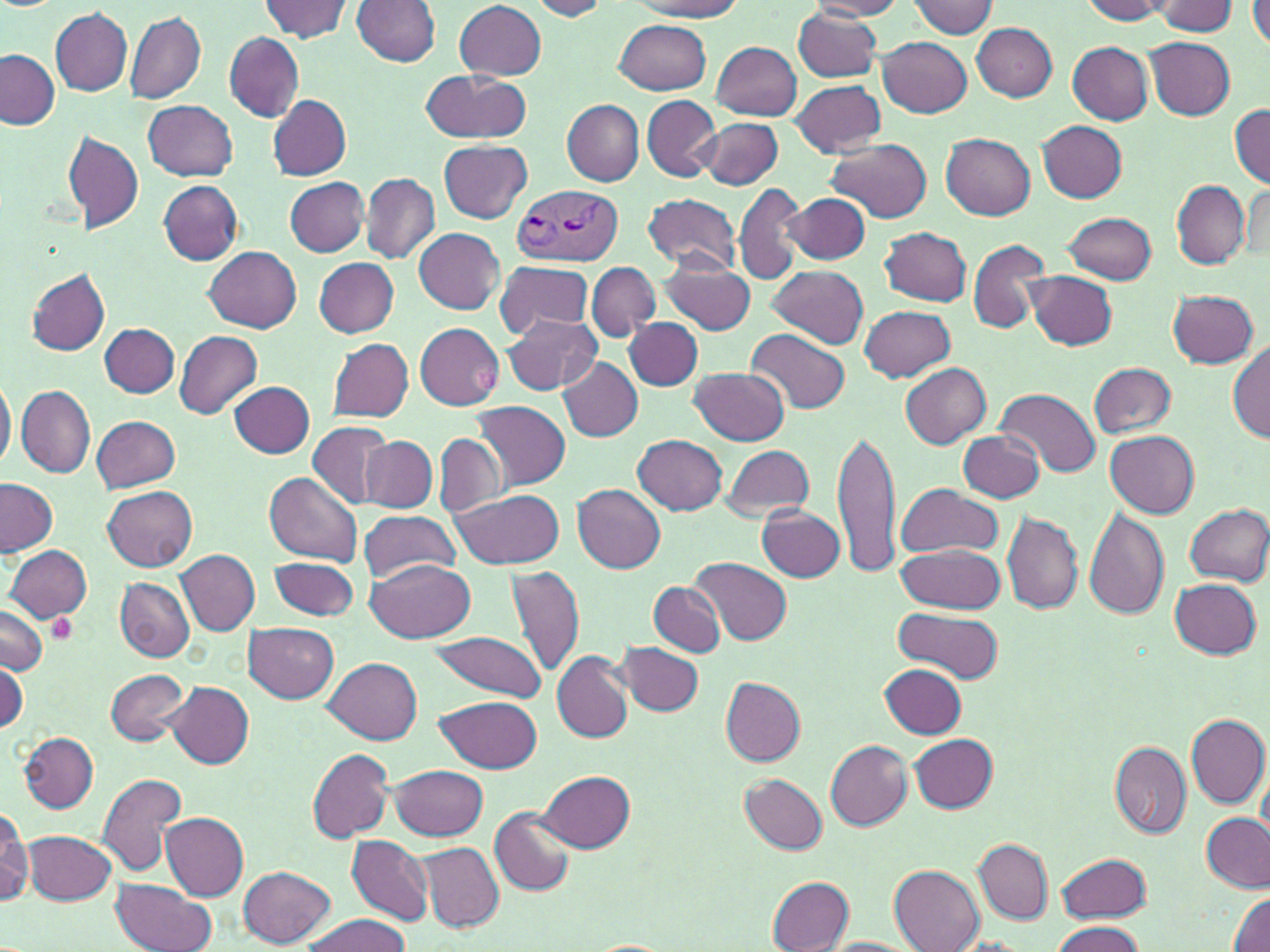 Approximate bounding boxes as named x1/y1/x2/y2 corners in pixels. Plasmodium vivax-infected red blood cell locations: (x1=509, y1=183, x2=621, y2=267). Uninfected red blood cell locations: (x1=261, y1=0, x2=352, y2=42), (x1=352, y1=0, x2=440, y2=66), (x1=528, y1=0, x2=610, y2=20), (x1=631, y1=0, x2=744, y2=19), (x1=809, y1=0, x2=906, y2=19), (x1=1080, y1=0, x2=1171, y2=23), (x1=1249, y1=0, x2=1270, y2=48), (x1=909, y1=1, x2=997, y2=37), (x1=1152, y1=1, x2=1239, y2=36), (x1=455, y1=2, x2=546, y2=78), (x1=793, y1=7, x2=882, y2=82), (x1=51, y1=8, x2=132, y2=96), (x1=125, y1=11, x2=206, y2=104), (x1=615, y1=19, x2=711, y2=93), (x1=972, y1=23, x2=1057, y2=101), (x1=223, y1=31, x2=303, y2=122), (x1=878, y1=35, x2=972, y2=118), (x1=1144, y1=38, x2=1235, y2=120), (x1=712, y1=41, x2=801, y2=120), (x1=1067, y1=42, x2=1153, y2=123), (x1=0, y1=50, x2=59, y2=130), (x1=420, y1=69, x2=533, y2=144), (x1=790, y1=80, x2=886, y2=156), (x1=642, y1=95, x2=720, y2=180), (x1=270, y1=96, x2=352, y2=179), (x1=144, y1=100, x2=238, y2=181), (x1=563, y1=100, x2=645, y2=185), (x1=1230, y1=103, x2=1270, y2=189), (x1=698, y1=117, x2=783, y2=190), (x1=1038, y1=121, x2=1127, y2=202), (x1=61, y1=129, x2=145, y2=234), (x1=942, y1=134, x2=1036, y2=219), (x1=826, y1=138, x2=931, y2=222), (x1=439, y1=139, x2=533, y2=224), (x1=361, y1=173, x2=439, y2=263), (x1=284, y1=176, x2=370, y2=257), (x1=734, y1=180, x2=809, y2=285), (x1=158, y1=181, x2=242, y2=264), (x1=1171, y1=181, x2=1250, y2=268), (x1=784, y1=192, x2=869, y2=264), (x1=643, y1=193, x2=742, y2=274), (x1=1063, y1=212, x2=1155, y2=284), (x1=881, y1=226, x2=973, y2=306), (x1=414, y1=228, x2=503, y2=313), (x1=968, y1=239, x2=1050, y2=333), (x1=205, y1=247, x2=302, y2=332), (x1=313, y1=257, x2=399, y2=337), (x1=493, y1=259, x2=596, y2=340), (x1=659, y1=259, x2=755, y2=336), (x1=587, y1=262, x2=659, y2=341), (x1=767, y1=265, x2=867, y2=350), (x1=25, y1=269, x2=111, y2=356), (x1=1024, y1=271, x2=1117, y2=350), (x1=1168, y1=289, x2=1258, y2=368), (x1=860, y1=305, x2=956, y2=382), (x1=625, y1=306, x2=708, y2=466), (x1=502, y1=313, x2=602, y2=395), (x1=626, y1=318, x2=702, y2=391), (x1=415, y1=323, x2=503, y2=409), (x1=99, y1=324, x2=180, y2=397), (x1=747, y1=329, x2=852, y2=415), (x1=174, y1=330, x2=262, y2=419), (x1=327, y1=338, x2=414, y2=421), (x1=1229, y1=339, x2=1270, y2=443), (x1=559, y1=358, x2=643, y2=440), (x1=1088, y1=361, x2=1177, y2=439), (x1=901, y1=363, x2=991, y2=448), (x1=691, y1=366, x2=790, y2=445), (x1=0, y1=371, x2=15, y2=477), (x1=231, y1=380, x2=314, y2=458), (x1=16, y1=386, x2=96, y2=479), (x1=996, y1=389, x2=1098, y2=478), (x1=474, y1=401, x2=570, y2=490), (x1=92, y1=416, x2=181, y2=493), (x1=309, y1=421, x2=396, y2=510), (x1=832, y1=425, x2=901, y2=580), (x1=1105, y1=429, x2=1200, y2=517), (x1=960, y1=431, x2=1047, y2=502), (x1=434, y1=433, x2=506, y2=517), (x1=632, y1=435, x2=728, y2=515), (x1=363, y1=436, x2=438, y2=512), (x1=719, y1=445, x2=816, y2=522), (x1=266, y1=471, x2=362, y2=564), (x1=0, y1=478, x2=56, y2=555), (x1=893, y1=482, x2=1002, y2=559), (x1=572, y1=483, x2=666, y2=573), (x1=103, y1=486, x2=198, y2=572), (x1=450, y1=488, x2=566, y2=568), (x1=1183, y1=504, x2=1270, y2=587), (x1=756, y1=506, x2=846, y2=582), (x1=357, y1=509, x2=463, y2=582), (x1=1083, y1=509, x2=1169, y2=619), (x1=1004, y1=510, x2=1082, y2=613), (x1=896, y1=543, x2=1007, y2=614), (x1=5, y1=545, x2=91, y2=623), (x1=177, y1=551, x2=259, y2=635), (x1=269, y1=556, x2=358, y2=621), (x1=365, y1=557, x2=476, y2=641), (x1=691, y1=559, x2=793, y2=646), (x1=503, y1=564, x2=586, y2=676), (x1=115, y1=578, x2=194, y2=662), (x1=1170, y1=578, x2=1263, y2=659), (x1=649, y1=582, x2=726, y2=657), (x1=0, y1=604, x2=48, y2=675), (x1=894, y1=607, x2=1004, y2=682), (x1=244, y1=623, x2=339, y2=704), (x1=426, y1=630, x2=548, y2=701), (x1=618, y1=642, x2=704, y2=716), (x1=552, y1=651, x2=633, y2=743), (x1=1, y1=658, x2=27, y2=734), (x1=324, y1=659, x2=423, y2=745), (x1=881, y1=664, x2=965, y2=737), (x1=105, y1=668, x2=188, y2=745), (x1=721, y1=678, x2=806, y2=765), (x1=166, y1=682, x2=255, y2=769), (x1=439, y1=696, x2=541, y2=773), (x1=1186, y1=713, x2=1269, y2=809), (x1=19, y1=731, x2=99, y2=813), (x1=910, y1=734, x2=998, y2=812), (x1=824, y1=737, x2=1003, y2=821), (x1=825, y1=740, x2=911, y2=830), (x1=1109, y1=741, x2=1192, y2=839), (x1=308, y1=750, x2=392, y2=842), (x1=391, y1=764, x2=488, y2=840), (x1=539, y1=770, x2=635, y2=852), (x1=98, y1=772, x2=187, y2=878), (x1=740, y1=772, x2=828, y2=854), (x1=489, y1=808, x2=576, y2=897), (x1=1200, y1=811, x2=1270, y2=893), (x1=1, y1=814, x2=31, y2=909), (x1=160, y1=814, x2=248, y2=900), (x1=24, y1=830, x2=116, y2=905), (x1=346, y1=834, x2=434, y2=926), (x1=973, y1=839, x2=1052, y2=923), (x1=419, y1=843, x2=502, y2=932), (x1=1056, y1=852, x2=1151, y2=923), (x1=238, y1=865, x2=335, y2=948), (x1=889, y1=865, x2=984, y2=951), (x1=767, y1=876, x2=855, y2=951), (x1=110, y1=878, x2=217, y2=952), (x1=1228, y1=889, x2=1270, y2=952), (x1=299, y1=915, x2=414, y2=951), (x1=1048, y1=920, x2=1145, y2=952), (x1=820, y1=937, x2=921, y2=952). Platelet locations: (x1=468, y1=366, x2=500, y2=396), (x1=50, y1=616, x2=73, y2=645). Slide-level diagnosis: Plasmodium vivax. Optical microscopy. May-Grünwald-Giemsa stain. Image is 1270×952 pixels. One field of a larger specimen. Captured at 1000x magnification. Thin blood film.